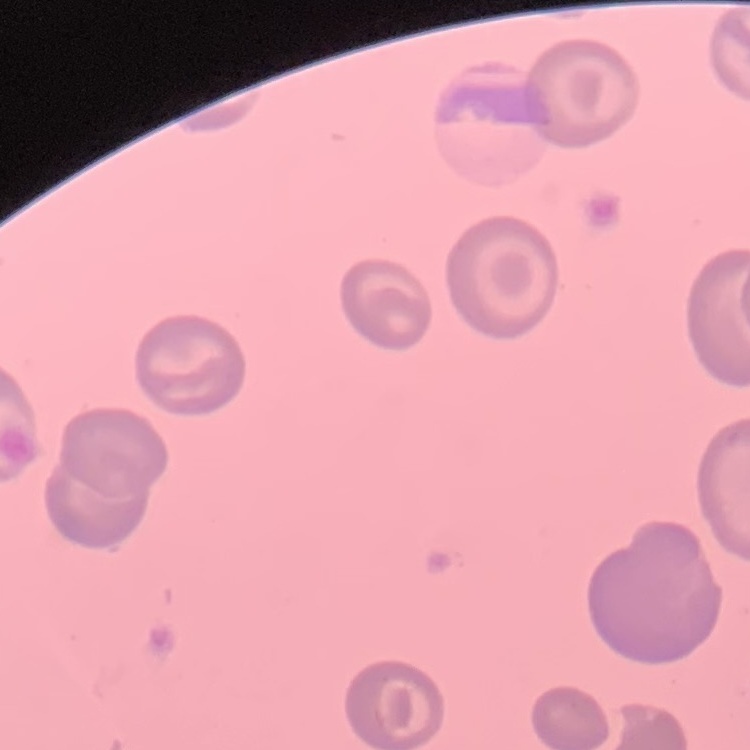
The red blood cells exhibit no rouleaux formation. Stained with either Field's or Giemsa. Square crop of a larger photomicrograph. Thin blood smear.